Identify the parasite.
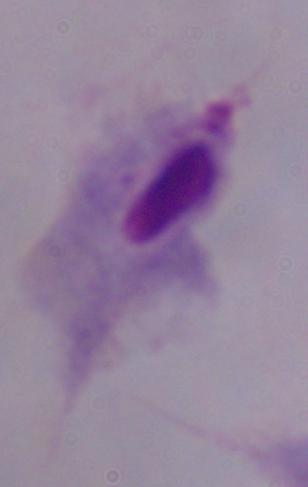
A trichomonad.

magnification = 1000x
modality = photomicrograph